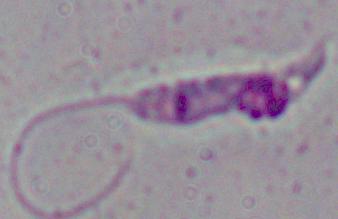
Summary:
  - Modality: photomicrograph
  - Magnification: 1000x
  - Identification: Leishmania